Classify this cell by malaria status.
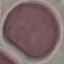

It is uninfected.

{
  "preparation": "thin blood smear",
  "capture": "smartphone through the microscope eyepiece",
  "image_type": "cell patch, automatically extracted from a larger field of view and resized to 64 × 64 pixels",
  "stain": "Giemsa"
}